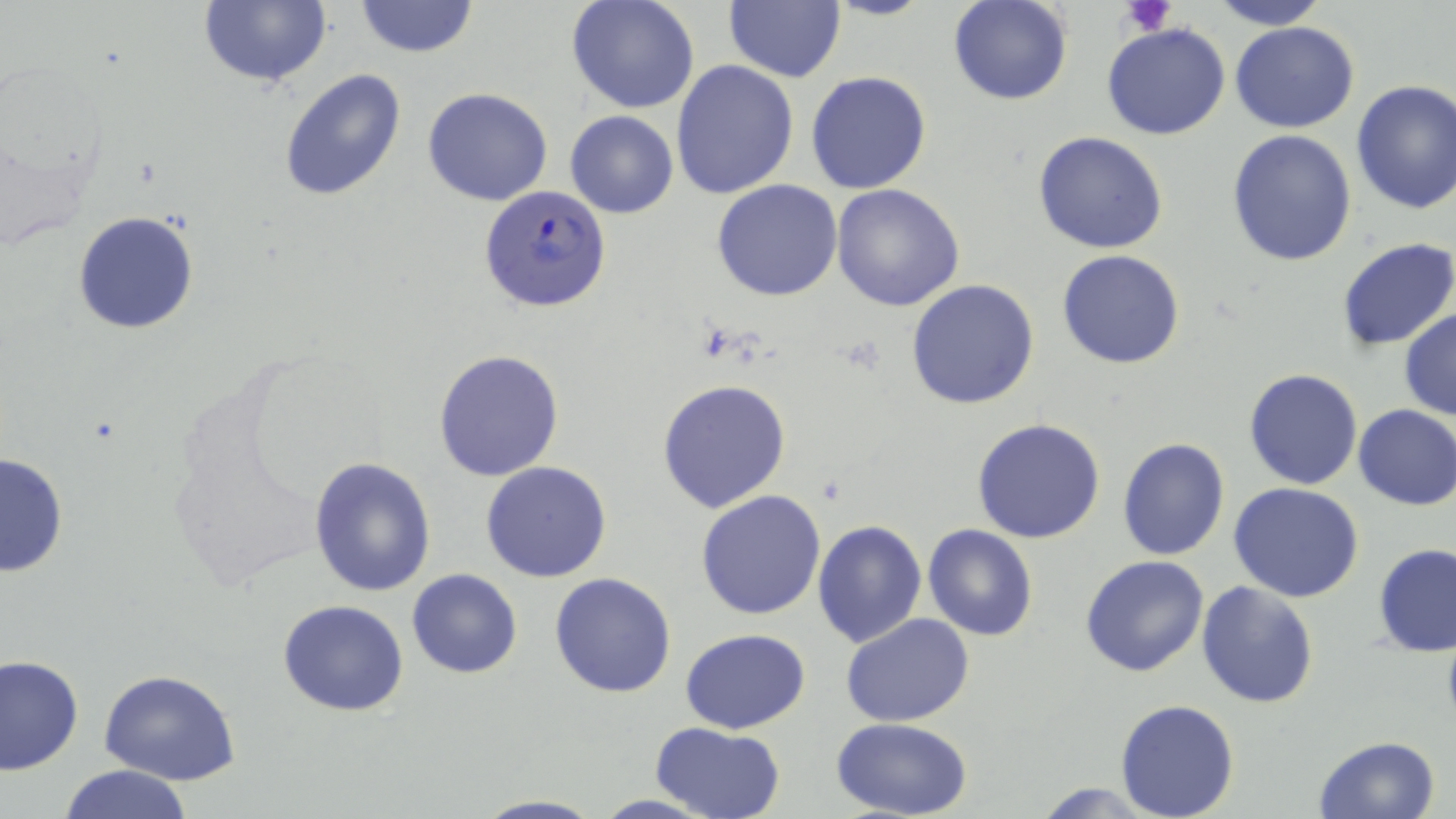
slide-level diagnosis = Plasmodium falciparum
modality = light microscopy
Plasmodium falciparum-infected red blood cell locations = approximate bounding boxes as (x1, y1, x2, y2) in pixels: (479, 183, 613, 313)
platelet locations = approximate bounding boxes as (x1, y1, x2, y2) in pixels: (1122, 0, 1178, 37)
uninfected red blood cell locations = approximate bounding boxes as (x1, y1, x2, y2) in pixels: (198, 0, 332, 89), (354, 0, 479, 57), (567, 0, 699, 114), (948, 0, 1074, 105), (1211, 0, 1329, 29), (722, 2, 846, 83), (1230, 21, 1359, 133), (1103, 22, 1231, 142), (670, 60, 799, 200), (280, 68, 406, 202), (806, 71, 932, 193), (1350, 80, 1456, 215), (423, 88, 551, 206), (565, 110, 678, 219), (1227, 129, 1358, 267), (1032, 131, 1170, 255), (712, 180, 842, 301), (831, 185, 965, 312), (73, 210, 199, 334), (1336, 238, 1456, 352), (1057, 249, 1187, 369), (905, 279, 1040, 410), (1399, 308, 1456, 422), (433, 349, 563, 480), (1243, 368, 1365, 490), (657, 378, 791, 513), (1352, 403, 1456, 511), (970, 418, 1106, 543), (1117, 437, 1230, 559), (1, 451, 69, 576), (308, 456, 436, 595), (481, 460, 613, 583), (1229, 482, 1363, 603), (695, 488, 827, 619), (811, 518, 927, 649), (923, 525, 1037, 642), (1374, 543, 1455, 658), (1081, 556, 1210, 678), (407, 569, 522, 678), (549, 572, 678, 698), (1196, 581, 1320, 710), (278, 600, 408, 716), (841, 613, 976, 728), (681, 627, 810, 735), (2, 654, 83, 775), (99, 671, 242, 786), (1115, 699, 1241, 818), (829, 718, 976, 818), (649, 721, 787, 818), (1313, 736, 1441, 819), (58, 764, 194, 819), (471, 794, 605, 818), (591, 795, 720, 817)
field of view = one of a larger specimen
preparation = thin blood smear
stain = May-Grünwald-Giemsa
magnification = 1000x
image size = 1456×819 pixels